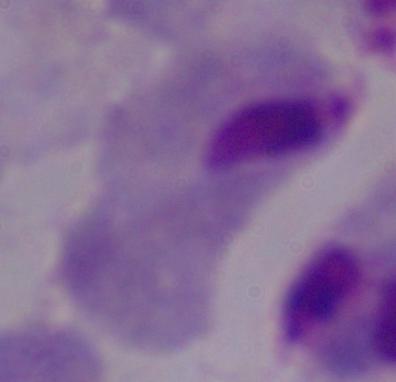

Summary:
  - Modality: photomicrograph
  - Magnification: 1000x
  - Identification: trichomonad